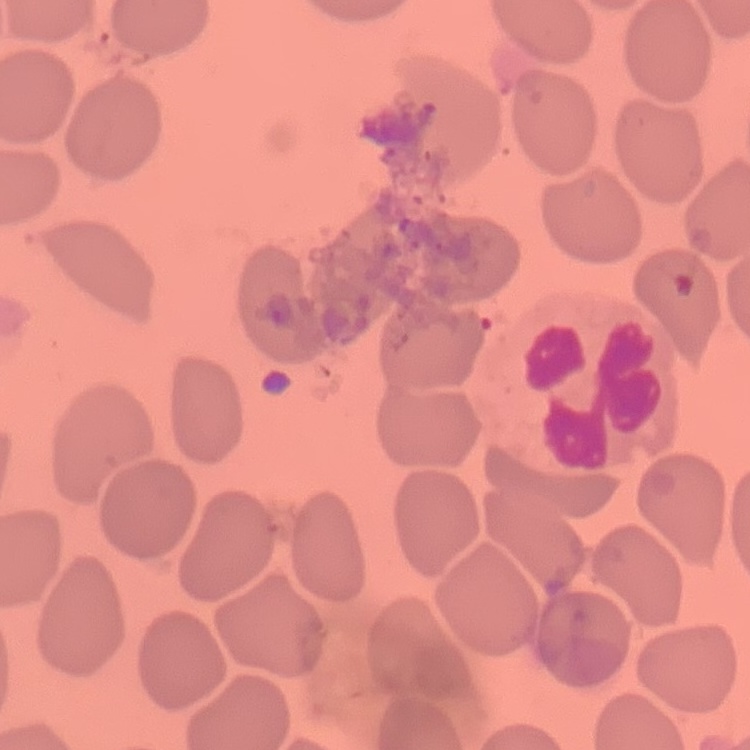
Summary:
  - Erythrocyte morphology: no rouleaux formation
  - Image type: square crop of a larger photomicrograph
  - Preparation: thin blood smear
  - Stain: Field's or Giemsa